Assess this cell for malaria.
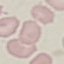
Uninfected.

Thin blood smear. Cell patch, automatically extracted from a larger field of view and resized to 64 × 64 pixels. Giemsa-stained preparation. Photographed with a smartphone camera at the microscope eyepiece.